State which parasite is depicted.
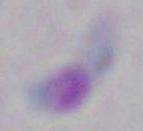

This is Toxoplasma gondii.

{
  "modality": "photomicrograph",
  "magnification": "1000x"
}